Give the position of every leukocyte visible.
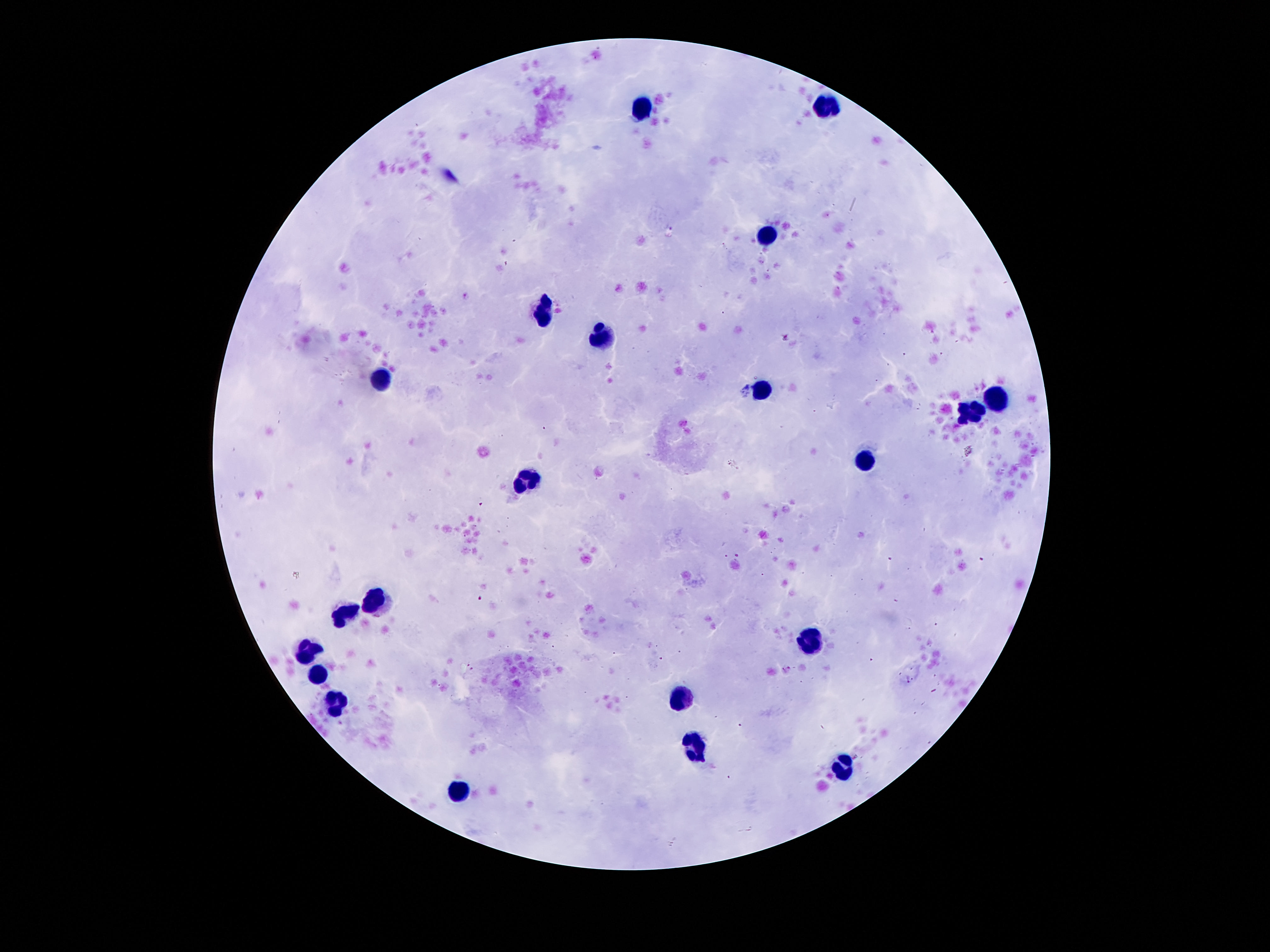
Approximate centers as (x, y) in pixels.
Leukocytes: (828, 104), (640, 108), (766, 234), (539, 312), (601, 337), (380, 379), (762, 391), (994, 397), (970, 413), (864, 459), (523, 479), (373, 600), (344, 613), (811, 641), (304, 648), (318, 675), (678, 696), (335, 699), (693, 749), (844, 769), (459, 792).

Thick peripheral-blood smear. Giemsa stain. Single field of view. Smartphone photograph taken through the microscope eyepiece. Image is 1270×952 pixels. 100x magnification. Patient malaria status: uninfected.